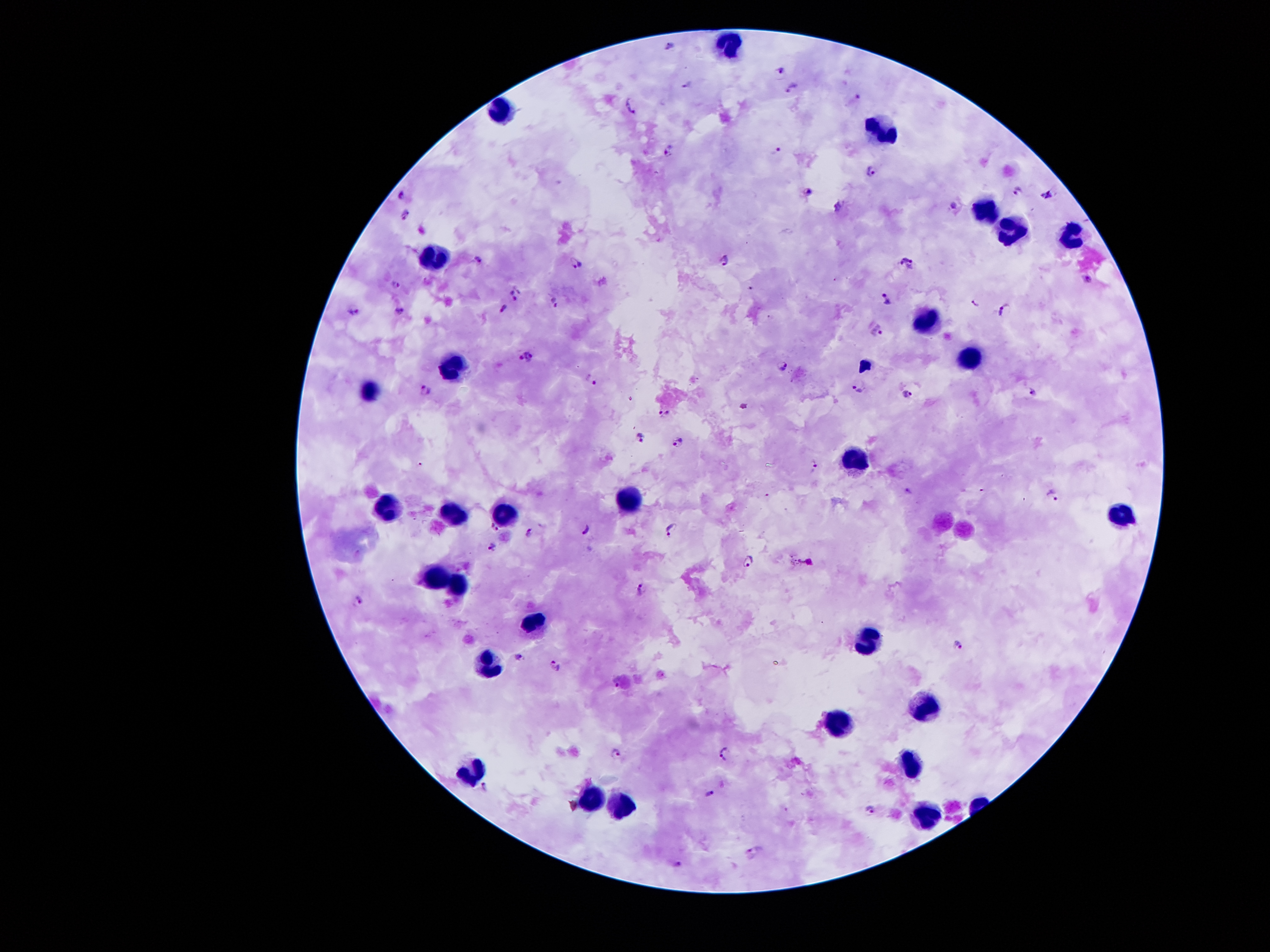
Approximate centers as [x, y] in pixels.
Summary:
  - Plasmodium parasite locations: [670, 45], [781, 68], [687, 83], [792, 87], [857, 96], [631, 106], [777, 151], [667, 152], [869, 169], [1018, 191], [809, 192], [401, 193], [1047, 194], [837, 205], [954, 205], [405, 214], [900, 258], [477, 259], [725, 261], [576, 262], [911, 267], [1086, 278], [395, 284], [514, 294], [886, 300], [553, 302], [974, 304], [1003, 308], [400, 310], [503, 310], [355, 311], [879, 332], [529, 358], [782, 365], [591, 379], [858, 388], [426, 390], [908, 392], [1034, 393], [664, 413], [638, 438], [677, 440], [814, 466], [907, 491], [1053, 494], [493, 526], [587, 527], [672, 529], [529, 534], [491, 547], [749, 560], [642, 589], [356, 600], [958, 647], [519, 656], [555, 664], [615, 680], [617, 753], [724, 755], [485, 785], [711, 792], [870, 810], [752, 852], [679, 865]
  - Leukocyte locations: [724, 45], [505, 118], [881, 128], [983, 209], [1012, 230], [1071, 234], [437, 254], [925, 316], [968, 356], [452, 364], [369, 390], [853, 457], [628, 498], [386, 507], [447, 511], [502, 511], [1119, 514], [432, 575], [454, 588], [536, 618], [866, 638], [486, 665], [924, 706], [841, 726], [912, 766], [476, 770], [592, 796], [621, 803], [927, 817]
  - Capture: smartphone camera through the microscope eyepiece
  - Magnification: 100x
  - Image size: 1270×952 pixels
  - Preparation: thick peripheral-blood smear
  - Patient malaria status: positive for Plasmodium falciparum
  - Field of view: one from this slide
  - Stain: Giemsa